Report the malaria status of this cell.
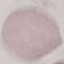
Uninfected.

stain = Giemsa
image type = automatically extracted cell patch, resized to 64 × 64 pixels
capture = smartphone camera at the microscope eyepiece
preparation = thin blood film